Report the malaria status of this cell.
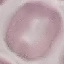
It is uninfected.

Summary:
  - Capture: smartphone through the microscope eyepiece
  - Stain: Giemsa
  - Preparation: thin smear
  - Image type: automatically extracted cell patch, resized to 64 × 64 pixels